State which parasite is depicted.
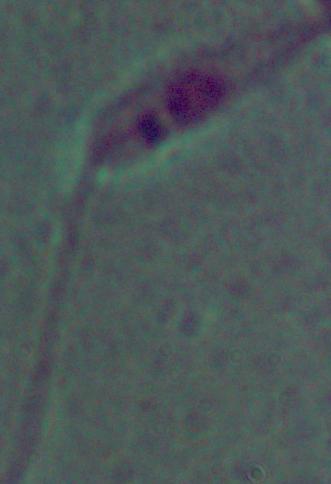

This is Leishmania.

Captured at 1000x magnification. Photomicrograph.